Assess this cell for malaria.
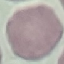

It is uninfected.

Summary:
  - Capture: smartphone through the microscope eyepiece
  - Stain: Giemsa
  - Image type: automatically extracted cell patch, resized to 64 × 64 pixels
  - Preparation: thin blood film